Identify the parasite.
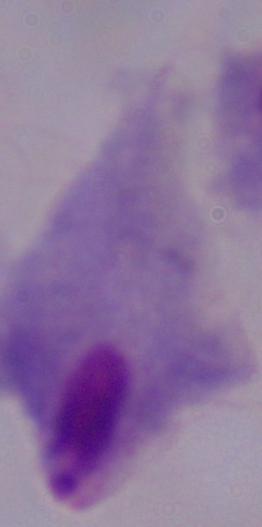

This is a trichomonad.

Summary:
  - Magnification: 1000x
  - Modality: photomicrograph